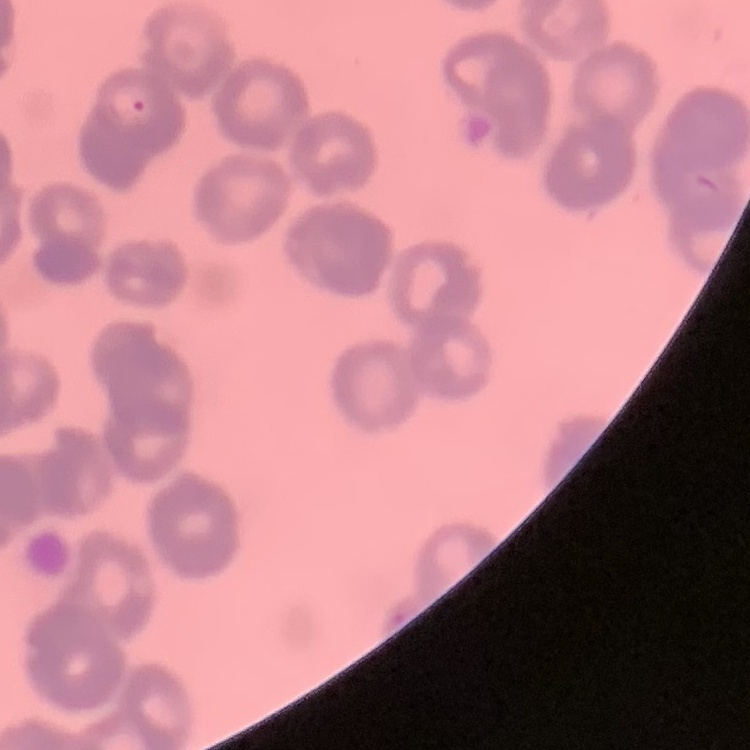
red blood cell morphology = rouleaux formation
image type = square crop of a larger photomicrograph
stain = Field's or Giemsa
preparation = thin blood smear